Identify the parasite.
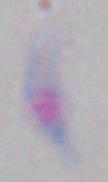

Toxoplasma gondii.

Summary:
  - Magnification: 1000x
  - Modality: photomicrograph